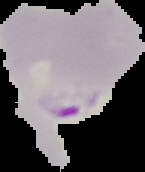
From a thin blood film. Malaria status: parasitized. Segmented cell region on a black background. Image is 145×172 pixels.